Identify the parasite.
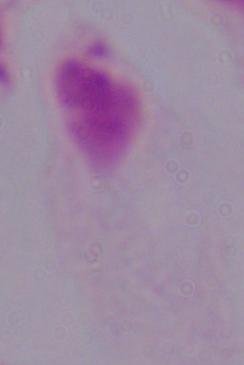

This is a trichomonad.

Photomicrograph. 1000x magnification.